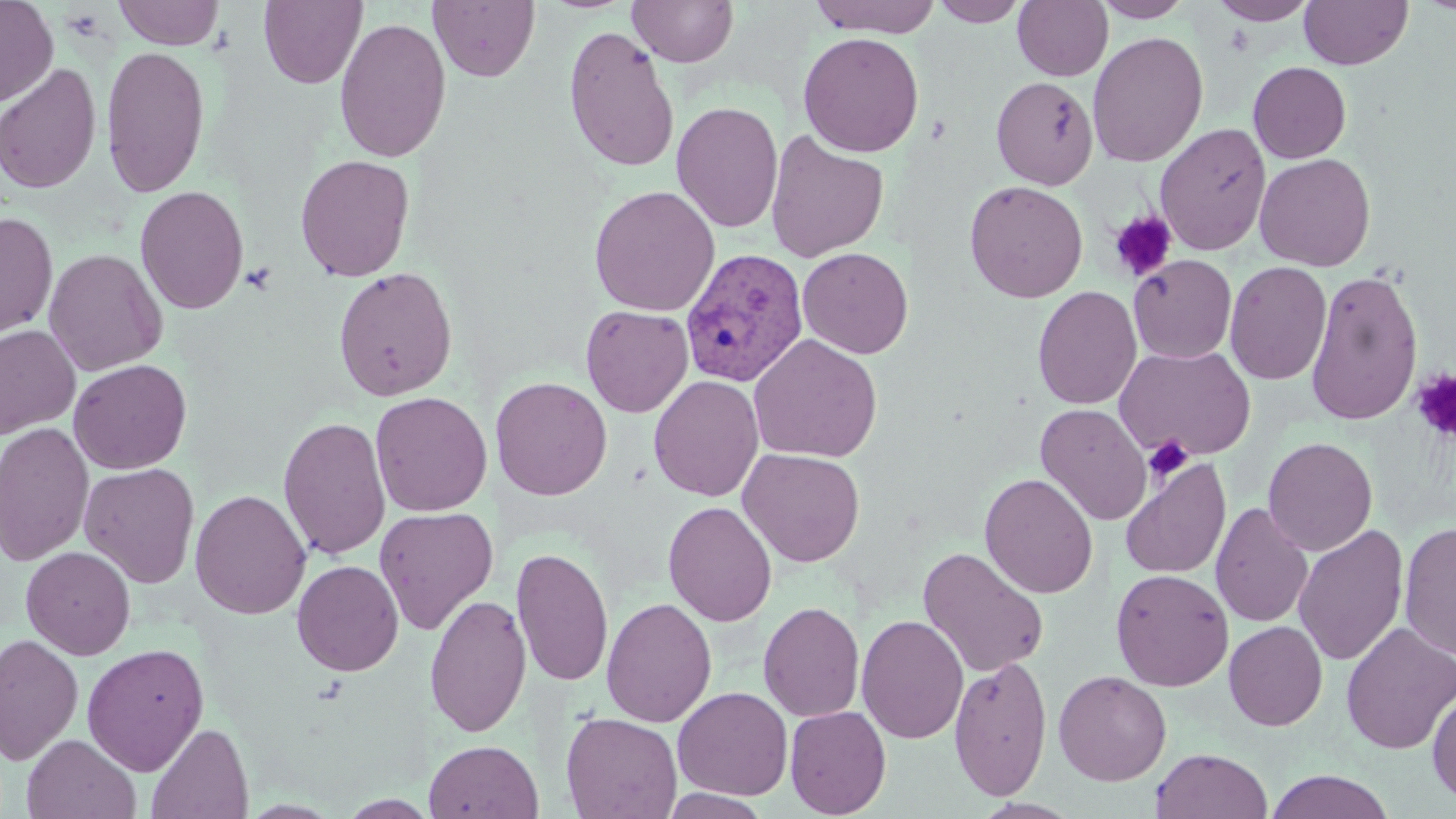
Approximate bounding boxes as [x1, y1, x2, y2] in pixels. Platelet locations: [1109, 211, 1177, 282], [241, 262, 277, 295], [1411, 369, 1456, 443], [1143, 435, 1194, 482]. Plasmodium vivax-infected red blood cell locations: [680, 247, 809, 387]. Uninfected red blood cell locations: [0, 0, 58, 106], [113, 0, 224, 49], [258, 0, 366, 88], [428, 0, 540, 82], [627, 0, 739, 67], [807, 0, 945, 37], [929, 0, 1030, 26], [1092, 0, 1195, 22], [1299, 0, 1413, 69], [1012, 1, 1113, 81], [1209, 1, 1318, 25], [333, 17, 452, 163], [563, 25, 680, 174], [798, 31, 925, 157], [1087, 31, 1209, 167], [101, 44, 210, 198], [1248, 61, 1351, 164], [0, 63, 102, 194], [991, 76, 1098, 190], [671, 101, 784, 233], [1154, 123, 1271, 256], [765, 130, 889, 263], [1254, 153, 1376, 271], [295, 154, 415, 282], [963, 180, 1088, 303], [134, 185, 249, 315], [588, 185, 720, 316], [1, 212, 58, 341], [798, 246, 914, 359], [43, 249, 167, 376], [1128, 254, 1237, 363], [1224, 260, 1332, 385], [333, 266, 458, 402], [1305, 268, 1424, 426], [1032, 286, 1142, 409], [580, 305, 694, 417], [0, 324, 80, 439], [747, 333, 883, 463], [1114, 343, 1257, 461], [68, 359, 192, 474], [648, 374, 764, 501], [490, 376, 613, 501], [369, 391, 493, 516], [1035, 403, 1152, 524], [278, 415, 391, 560], [0, 421, 95, 566], [1262, 437, 1378, 556], [738, 447, 865, 567], [1119, 456, 1231, 580], [79, 463, 200, 588], [979, 472, 1099, 598], [189, 489, 311, 619], [663, 501, 777, 627], [1210, 502, 1314, 628], [374, 506, 499, 635], [1398, 522, 1456, 661], [1292, 524, 1409, 667], [21, 545, 136, 660], [511, 546, 613, 687], [917, 546, 1050, 678], [292, 559, 404, 676], [1111, 569, 1233, 691], [424, 593, 532, 737], [601, 597, 717, 727], [759, 600, 865, 722], [856, 614, 970, 744], [1224, 621, 1328, 731], [1340, 622, 1455, 754], [0, 631, 84, 766], [82, 642, 209, 776], [949, 654, 1053, 800], [1053, 670, 1172, 786], [672, 686, 793, 800], [1427, 688, 1456, 807], [785, 705, 892, 818], [560, 711, 683, 819], [146, 723, 253, 818], [22, 734, 141, 818], [424, 739, 543, 819], [1151, 748, 1272, 819], [1264, 770, 1396, 819], [660, 789, 773, 818]. Slide-level diagnosis: Plasmodium vivax. 1000x magnification. May-Grünwald-Giemsa stain. Image is 1456×819 pixels. Light microscopy. One field of a larger specimen. Thin blood smear.